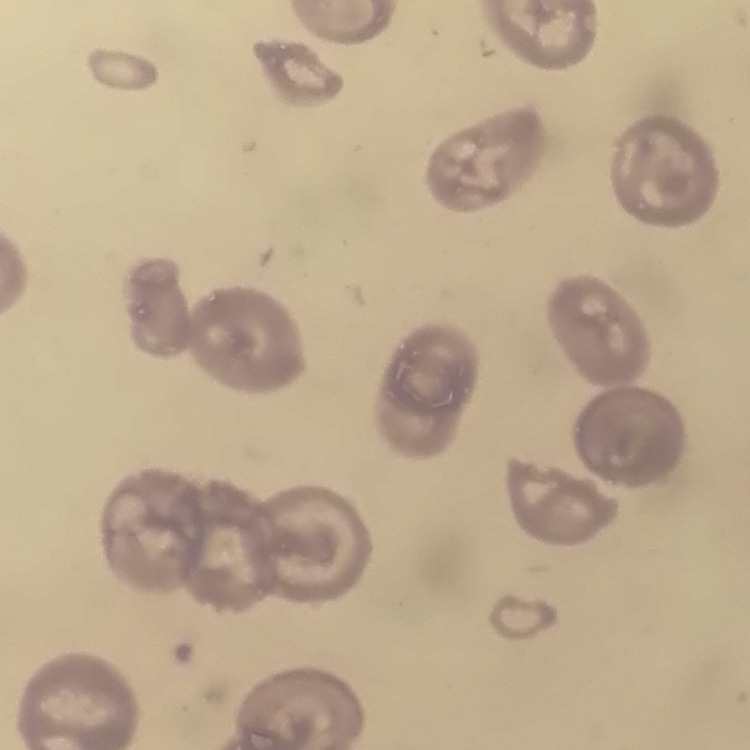
Summary:
  - Erythrocyte morphology: no rouleaux formation
  - Preparation: thin peripheral smear
  - Image type: square crop of a larger photomicrograph
  - Stain: Field's or Giemsa